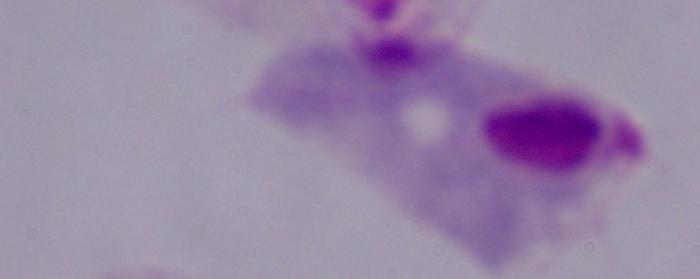

Photomicrograph. Captured at 1000x magnification. A trichomonad is seen.